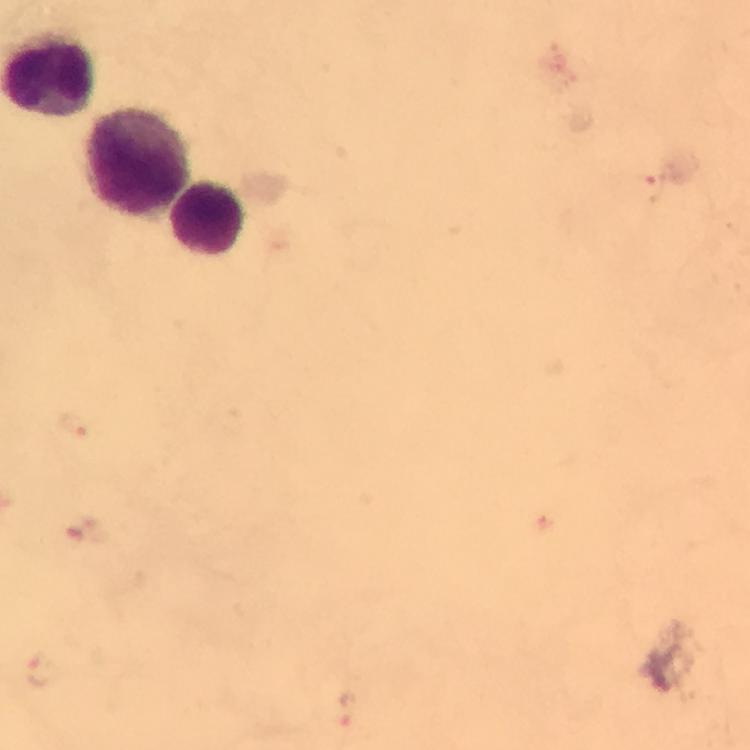 Approximate centers as (x, y) in pixels. Leukocyte locations: (138, 162), (208, 219). Plasmodium parasite locations: (654, 185), (74, 424), (44, 671), (347, 711). Cropped region of a single field of view. Photographed through the microscope with a smartphone camera. Giemsa-stained preparation. At 100x magnification. Thick smear. Image is 750×750 pixels. From a diagnostic examination for malaria. Immersion oil was used.